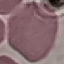 Malaria status: uninfected. Thin smear of blood. Giemsa-stained preparation. Cell patch, automatically extracted from a larger field of view and resized to 64 × 64 pixels. Photographed with a smartphone camera at the microscope eyepiece.